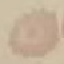
{
  "malaria_status": "uninfected",
  "image_type": "cell patch, automatically extracted from a larger field of view and resized to 64 × 64 pixels",
  "capture": "smartphone through the microscope eyepiece",
  "preparation": "thin blood film",
  "stain": "Giemsa"
}